Name the blood parasite species.
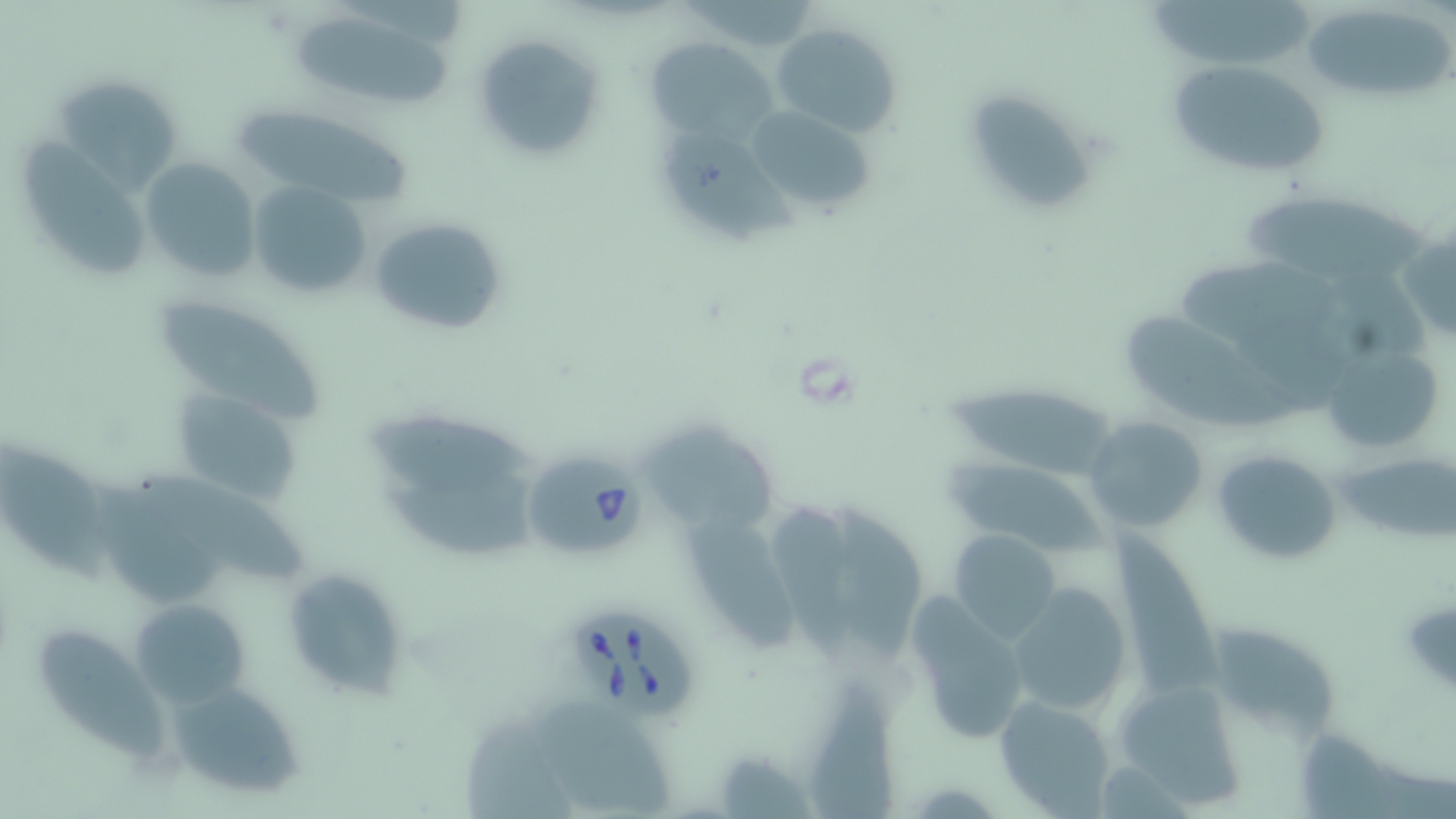
Babesia divergens.

Summary:
  - Coordinate format: approximate bounding boxes as named x1/y1/x2/y2 corners in pixels
  - Babesia divergens-infected red blood cell locations: (x1=524, y1=456, x2=647, y2=556), (x1=570, y1=611, x2=698, y2=720)
  - Uninfected red blood cell locations: (x1=1149, y1=0, x2=1322, y2=62), (x1=1301, y1=7, x2=1453, y2=105), (x1=298, y1=17, x2=453, y2=102), (x1=771, y1=22, x2=901, y2=137), (x1=473, y1=31, x2=607, y2=163), (x1=648, y1=38, x2=776, y2=145), (x1=1167, y1=59, x2=1332, y2=183), (x1=60, y1=75, x2=175, y2=200), (x1=970, y1=90, x2=1097, y2=211), (x1=745, y1=104, x2=877, y2=219), (x1=226, y1=108, x2=412, y2=200), (x1=664, y1=127, x2=797, y2=249), (x1=25, y1=139, x2=145, y2=276), (x1=139, y1=157, x2=262, y2=283), (x1=248, y1=179, x2=373, y2=303), (x1=1243, y1=190, x2=1422, y2=276), (x1=367, y1=213, x2=509, y2=338), (x1=1397, y1=226, x2=1456, y2=344), (x1=1186, y1=256, x2=1337, y2=340), (x1=153, y1=294, x2=326, y2=419), (x1=1124, y1=307, x2=1297, y2=430), (x1=1323, y1=340, x2=1449, y2=457), (x1=941, y1=386, x2=1123, y2=479), (x1=173, y1=388, x2=305, y2=510), (x1=362, y1=406, x2=545, y2=494), (x1=1086, y1=416, x2=1207, y2=532), (x1=644, y1=418, x2=774, y2=531), (x1=0, y1=439, x2=114, y2=585), (x1=1211, y1=447, x2=1343, y2=567), (x1=1334, y1=450, x2=1456, y2=544), (x1=948, y1=459, x2=1107, y2=557), (x1=140, y1=468, x2=307, y2=580), (x1=90, y1=470, x2=223, y2=606), (x1=374, y1=479, x2=549, y2=559), (x1=777, y1=501, x2=852, y2=674), (x1=839, y1=507, x2=920, y2=656), (x1=690, y1=516, x2=807, y2=657), (x1=1097, y1=518, x2=1225, y2=697), (x1=950, y1=529, x2=1061, y2=643), (x1=283, y1=567, x2=413, y2=704), (x1=1004, y1=578, x2=1135, y2=717), (x1=905, y1=596, x2=1032, y2=746), (x1=131, y1=598, x2=252, y2=706), (x1=1213, y1=616, x2=1336, y2=733), (x1=35, y1=621, x2=162, y2=763), (x1=1111, y1=678, x2=1250, y2=812), (x1=171, y1=681, x2=307, y2=802), (x1=807, y1=687, x2=906, y2=819), (x1=994, y1=694, x2=1118, y2=817), (x1=530, y1=703, x2=680, y2=817), (x1=466, y1=715, x2=578, y2=819)
  - Field of view: single
  - Stain: May-Grünwald-Giemsa
  - Preparation: thin blood film
  - Image size: 1456×819 pixels
  - Modality: light microscopy
  - Magnification: 1000x